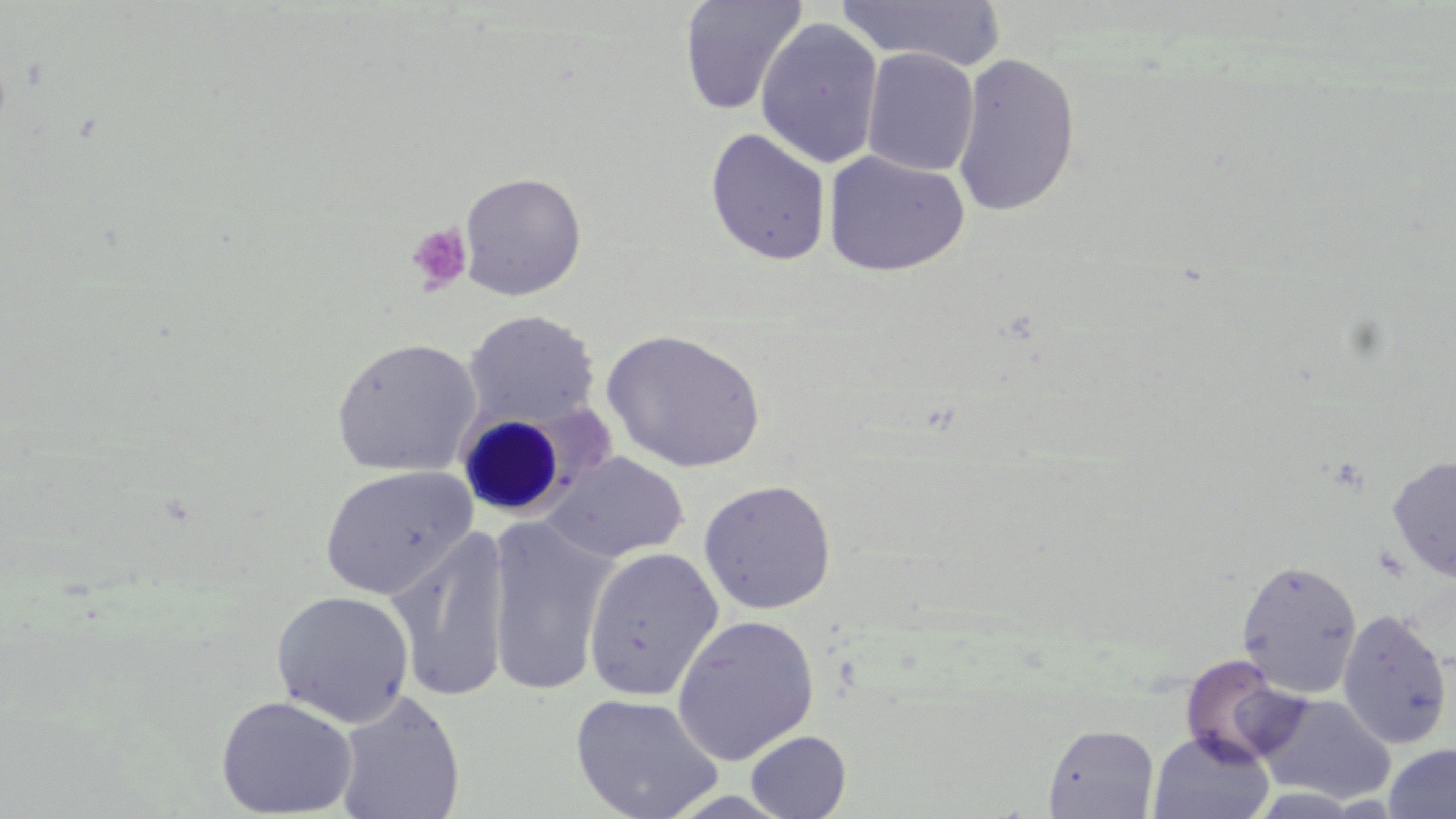
slide-level diagnosis = negative for blood parasites
white blood cell locations = approximate bounding boxes as [x1, y1, x2, y2] in pixels: [454, 410, 595, 520]
modality = optical microscopy
preparation = thin blood smear
platelet locations = approximate bounding boxes as [x1, y1, x2, y2] in pixels: [406, 222, 473, 295]
image size = 1456×819 pixels
magnification = 1000x
stain = May-Grünwald-Giemsa
uninfected red blood cell locations = approximate bounding boxes as [x1, y1, x2, y2] in pixels: [679, 0, 807, 115], [835, 1, 1008, 72], [755, 17, 883, 170], [861, 48, 980, 177], [952, 52, 1081, 218], [705, 127, 831, 265], [822, 151, 970, 277], [458, 171, 587, 301], [463, 309, 599, 428], [601, 328, 766, 473], [331, 337, 483, 477], [542, 451, 688, 563], [1388, 454, 1456, 583], [319, 464, 477, 599], [698, 479, 837, 614], [485, 517, 616, 698], [387, 525, 512, 703], [582, 546, 723, 701], [1236, 558, 1362, 697], [270, 589, 416, 727], [1336, 609, 1453, 749], [672, 614, 820, 765], [1178, 654, 1306, 769], [335, 691, 465, 819], [1255, 692, 1396, 803], [570, 693, 725, 819], [215, 694, 358, 817], [1043, 723, 1158, 818], [745, 730, 852, 818], [1148, 730, 1274, 818], [1383, 742, 1456, 819]
field of view = one of a larger specimen